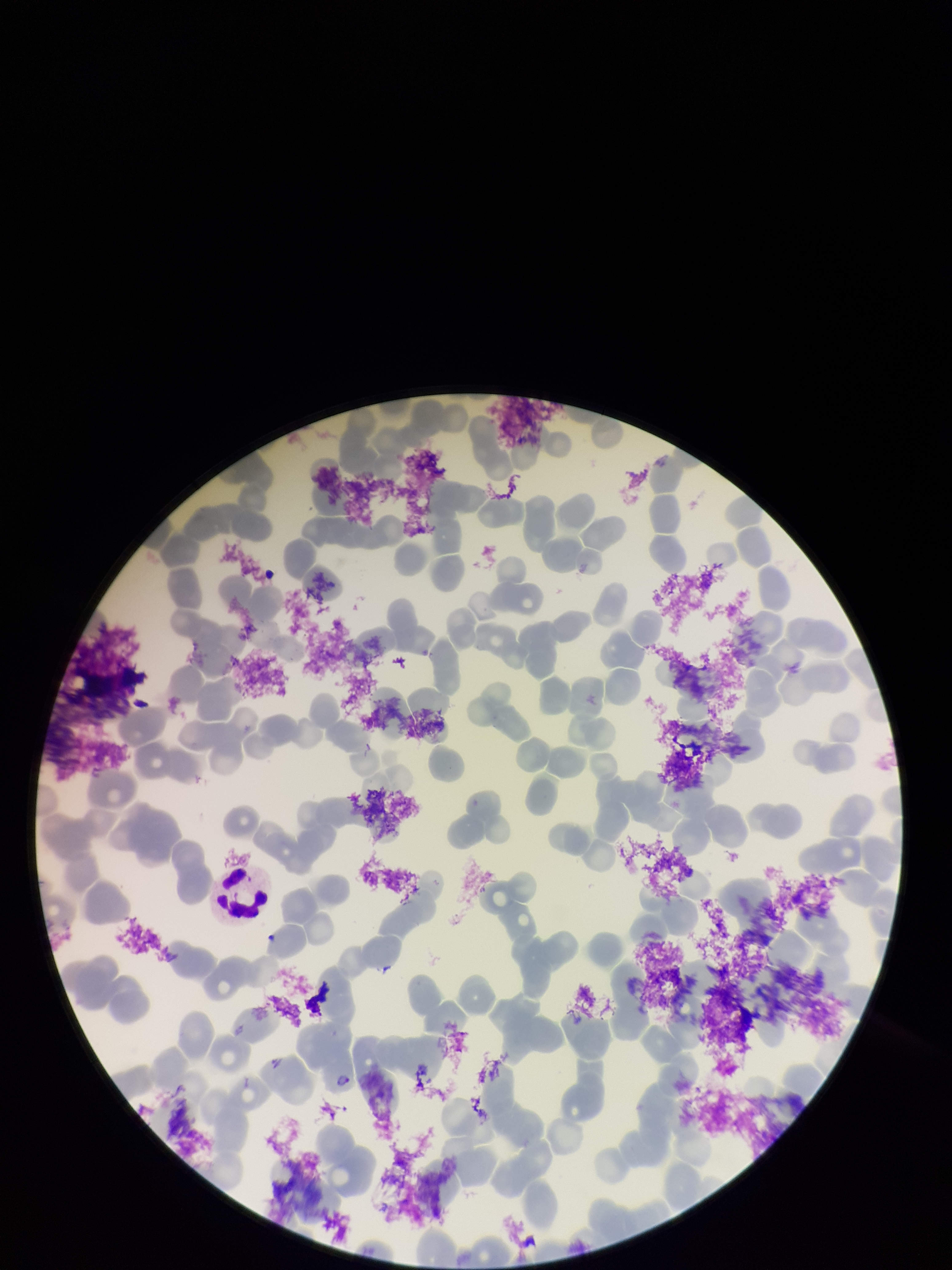
Summary:
  - Preparation: thin blood smear
  - Capture: smartphone photograph through the microscope eyepiece
  - Parasitized red blood cell count: 1
  - Stain: Giemsa
  - Image size: 952×1270 pixels
  - Field of view: single
  - Red blood cell count: 170
  - Parasitized red blood cells: detected
  - Patient malaria status: positive
  - Species reported for this patient: Plasmodium falciparum